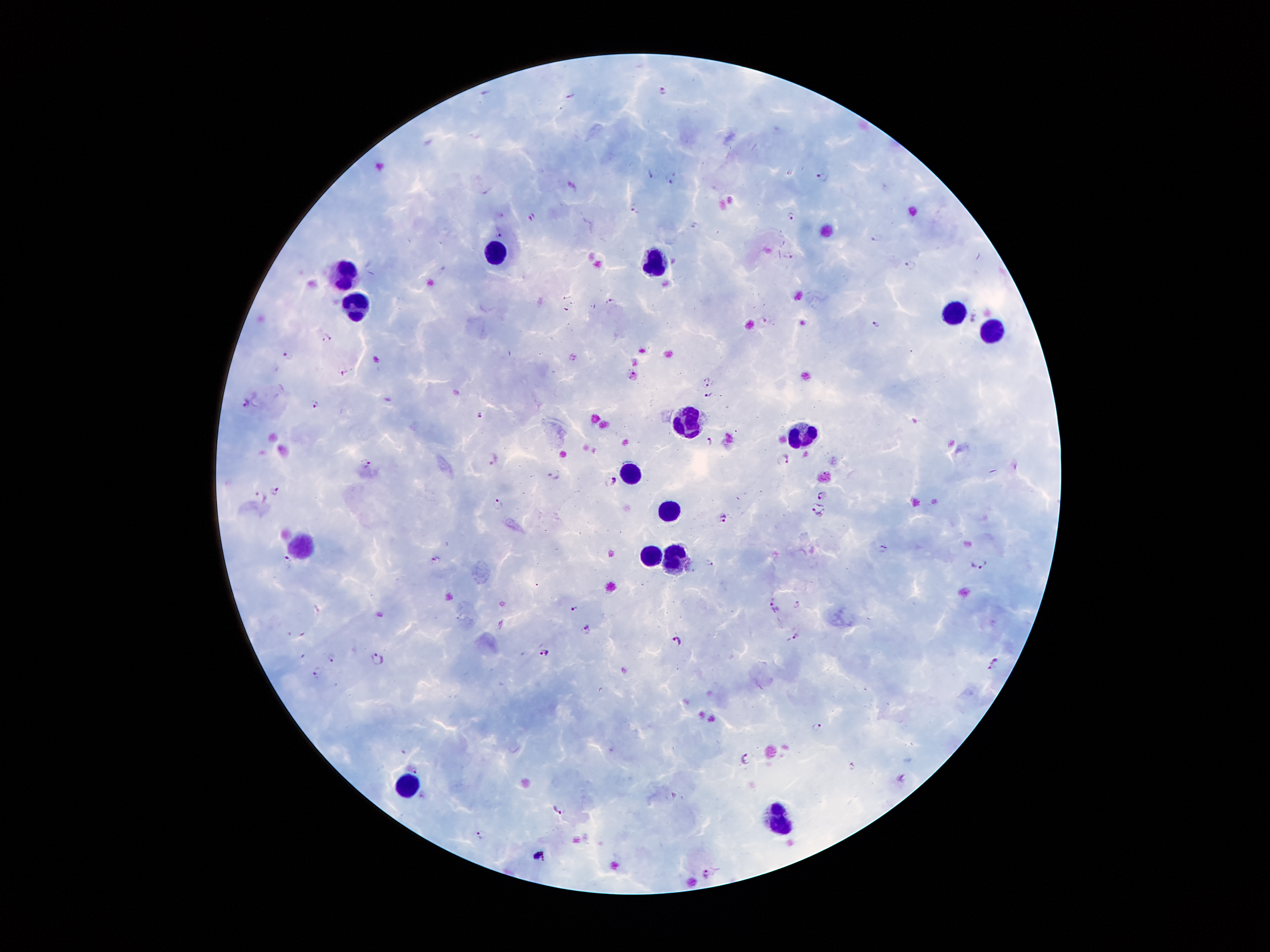

coordinate format = approximate centers as {x, y} in pixels
leukocyte locations = {494, 254}, {652, 264}, {344, 273}, {354, 304}, {953, 314}, {992, 328}, {688, 421}, {799, 437}, {631, 466}, {669, 509}, {302, 545}, {654, 554}, {678, 555}, {408, 784}, {779, 821}
Plasmodium parasite locations = {665, 91}, {652, 174}, {821, 176}, {669, 179}, {632, 205}, {792, 215}, {532, 217}, {497, 235}, {875, 238}, {788, 256}, {911, 264}, {613, 300}, {767, 318}, {876, 325}, {327, 337}, {290, 355}, {344, 372}, {707, 382}, {709, 393}, {246, 400}, {315, 403}, {480, 415}, {710, 441}, {492, 458}, {784, 458}, {365, 463}, {553, 475}, {615, 481}, {273, 491}, {823, 495}, {260, 496}, {498, 504}, {818, 509}, {724, 517}, {883, 548}, {436, 559}, {288, 560}, {708, 562}, {979, 563}, {798, 604}, {574, 608}, {774, 608}, {586, 629}, {795, 635}, {676, 640}, {545, 651}, {331, 657}, {377, 660}, {994, 665}, {318, 672}, {818, 728}, {748, 758}, {853, 766}, {414, 769}, {903, 778}, {557, 808}, {481, 833}, {539, 855}, {705, 873}
capture = smartphone through the microscope eyepiece
patient malaria status = positive for Plasmodium falciparum
preparation = thick peripheral-blood smear
stain = Giemsa
image size = 1270×952 pixels
magnification = 100x
field of view = one from this slide